Report the malaria status of this cell.
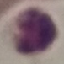

It is uninfected.

Giemsa-stained preparation. Thin blood film. Acquired by smartphone through the microscope eyepiece. Automatically extracted cell patch, resized to 64 × 64 pixels.